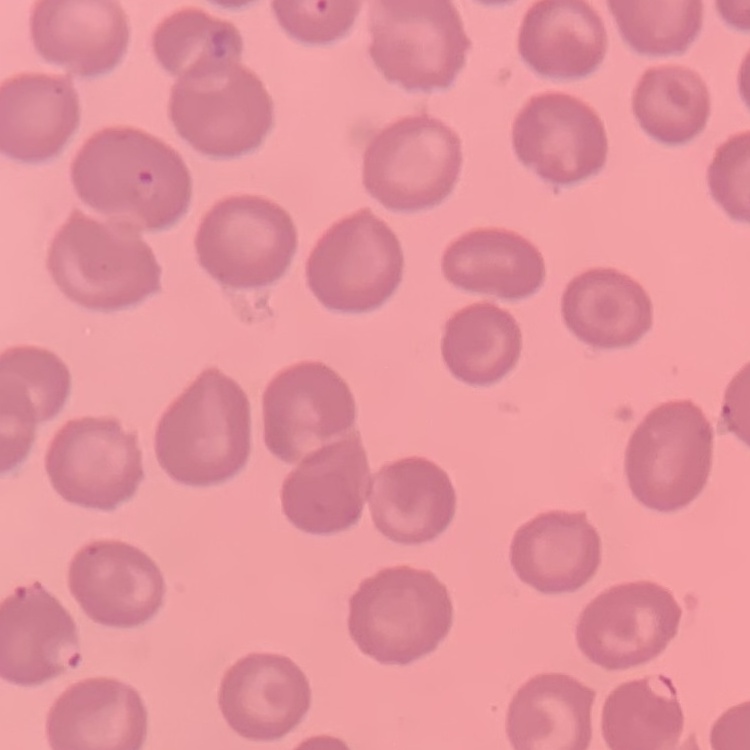

The erythrocytes show no rouleaux formation. Thin blood smear. Field's or Giemsa stain. Square crop of a larger photomicrograph.